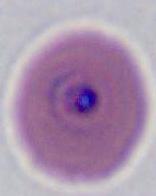

Summary:
  - Magnification: 400x or 1000x
  - Modality: micrograph
  - Identification: Plasmodium